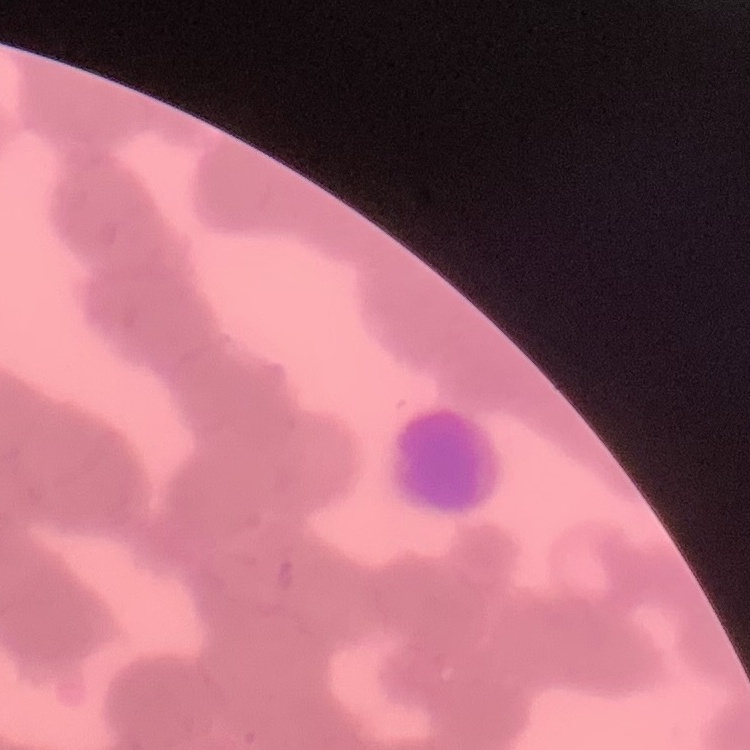 The red blood cells show rouleaux formation. One tile cut from a larger photomicrograph. Field's or Giemsa stain. Thin blood smear.